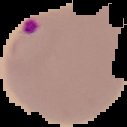

Summary:
  - Result: Plasmodium parasites identified
  - Image size: 127×127 pixels
  - Image type: segmented cell region with the area outside set to black
  - Preparation: thin blood smear